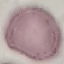
Summary:
  - Malaria status: uninfected
  - Preparation: thin blood smear
  - Capture: smartphone through the microscope eyepiece
  - Image type: cell patch, automatically extracted from a larger field of view and resized to 64 × 64 pixels
  - Stain: Giemsa